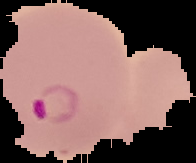
Summary:
  - Malaria status: parasitized
  - Preparation: thin blood smear
  - Image type: segmented cell region with the area outside set to black
  - Image size: 196×163 pixels